Comment on the morphology of the erythrocytes.
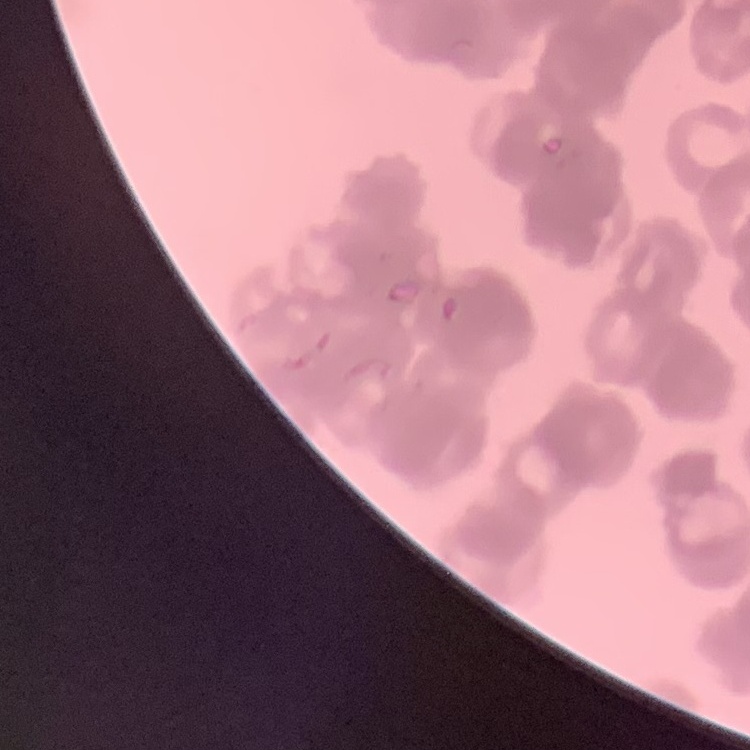

They show rouleaux formation.

Thin blood film. Stained with either Field's or Giemsa. Square crop of a larger photomicrograph.